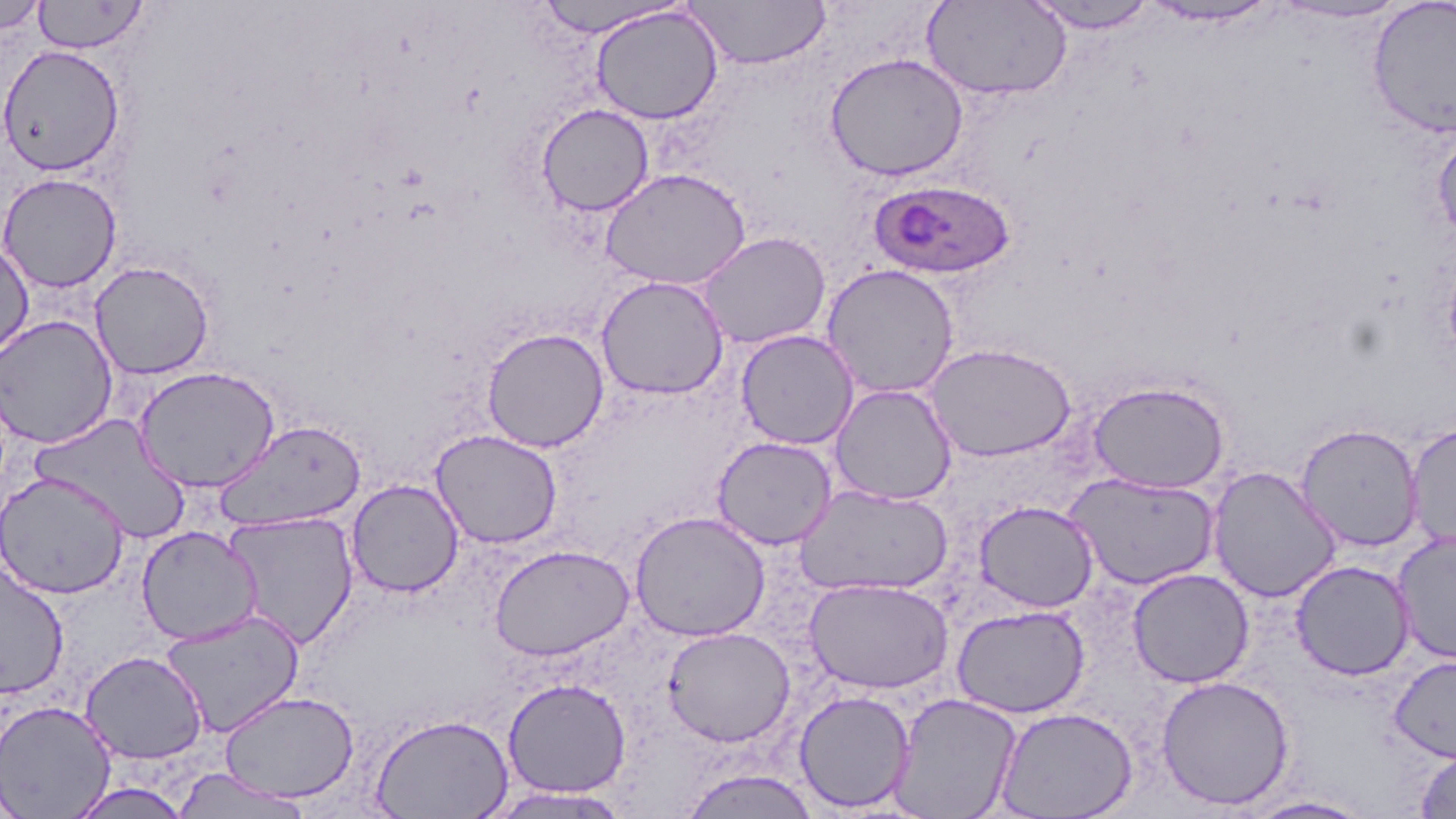
slide-level diagnosis = Plasmodium ovale
image size = 1456×819 pixels
uninfected red blood cell locations = approximate bounding boxes as (x1,y1)-(x2,y2) corner pairs in pixels: (0,0)-(47,34), (1023,0)-(1161,33), (1368,0)-(1456,138), (32,1)-(148,53), (531,1)-(689,37), (685,1)-(831,69), (923,1)-(1071,100), (1139,1)-(1281,28), (1273,1)-(1409,24), (590,5)-(724,125), (0,44)-(125,177), (825,53)-(968,180), (536,103)-(655,216), (1432,127)-(1456,245), (599,168)-(751,289), (0,173)-(122,293), (697,231)-(831,349), (0,240)-(35,362), (89,261)-(215,380), (821,264)-(960,399), (595,275)-(729,400), (0,315)-(118,449), (482,327)-(609,453), (736,330)-(858,450), (924,342)-(1076,463), (133,365)-(281,493), (1088,380)-(1229,493), (829,384)-(957,506), (28,413)-(191,542), (214,419)-(367,532), (1296,423)-(1425,553), (1406,423)-(1456,551), (430,429)-(563,549), (712,436)-(837,549), (1208,466)-(1341,603), (0,471)-(130,599), (1065,473)-(1220,590), (347,479)-(464,597), (796,484)-(953,596), (974,500)-(1099,613), (630,510)-(770,641), (222,511)-(359,649), (136,525)-(261,646), (1392,531)-(1456,666), (490,544)-(633,661), (1291,560)-(1415,680), (0,562)-(69,699), (1128,568)-(1254,688), (804,577)-(954,694), (952,605)-(1090,718), (159,609)-(305,738), (662,626)-(795,747), (80,651)-(208,764), (1389,654)-(1456,763), (1155,675)-(1294,810), (502,678)-(631,798), (219,690)-(359,802), (794,690)-(917,812), (889,693)-(1022,819), (0,699)-(116,818), (994,706)-(1138,818), (369,713)-(514,819), (1414,748)-(1456,818), (169,769)-(312,818), (679,769)-(821,819), (67,781)-(193,818), (482,787)-(633,818), (1240,795)-(1375,818)
modality = optical microscopy
Plasmodium ovale-infected red blood cell locations = approximate bounding boxes as (x1,y1)-(x2,y2) corner pairs in pixels: (869,179)-(1015,281)
magnification = 1000x
stain = May-Grünwald-Giemsa
preparation = thin blood film
field of view = single